Name the parasite shown.
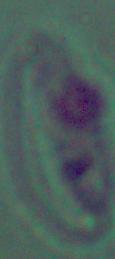

Leishmania.

Captured at 1000x magnification. Photomicrograph.